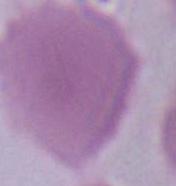
A red blood cell is shown. Captured at 1000x magnification. Photomicrograph.